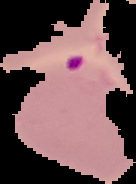
Summary:
  - Preparation: thin blood film
  - Image type: segmented cell region on a black background
  - Image size: 136×184 pixels
  - Malaria status: parasitized